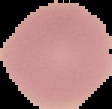
image type = cell region segmented out of the field of view; surrounding area masked to black
malaria status = uninfected
preparation = thin blood film
image size = 112×109 pixels